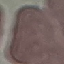

result: no malaria parasites seen
stain: Giemsa
image_type: cell patch, automatically extracted from a larger field of view and resized to 64 × 64 pixels
capture: smartphone camera at the microscope eyepiece
preparation: thin smear